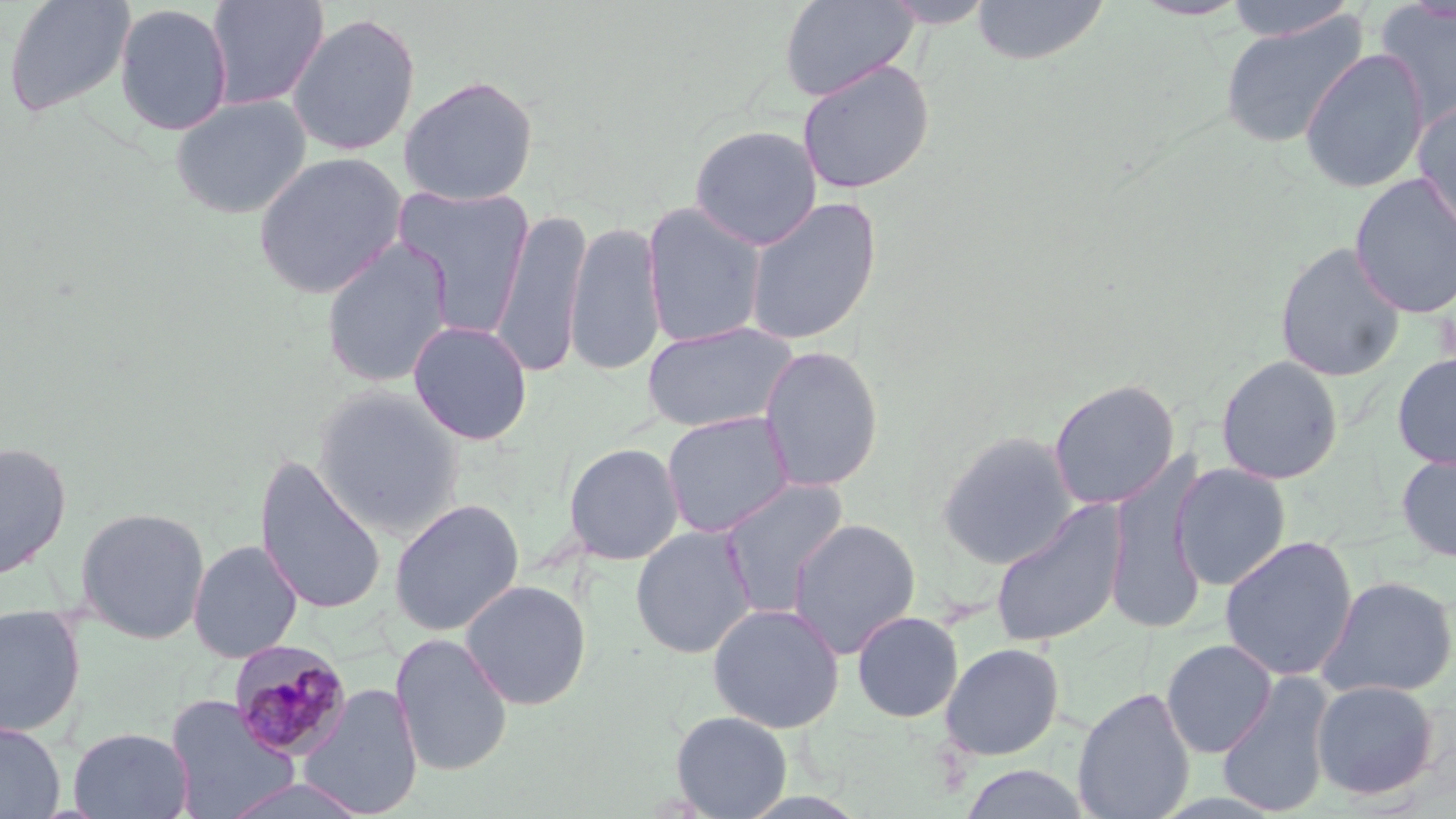
Approximate bounding boxes as (x1, y1, x2, y2) in pixels. Plasmodium malariae-infected red blood cell locations: (226, 639, 351, 761). Uninfected red blood cell locations: (3, 0, 136, 119), (778, 0, 918, 101), (971, 0, 1110, 66), (1221, 0, 1359, 41), (206, 1, 330, 110), (880, 1, 996, 29), (114, 3, 233, 136), (1375, 3, 1456, 129), (286, 11, 421, 156), (1219, 13, 1369, 149), (1299, 47, 1430, 193), (797, 59, 935, 195), (399, 75, 539, 206), (169, 94, 312, 219), (1413, 99, 1456, 239), (689, 124, 822, 250), (252, 151, 408, 299), (1349, 173, 1456, 318), (392, 184, 536, 336), (743, 195, 882, 346), (641, 202, 767, 349), (490, 207, 592, 379), (565, 221, 666, 378), (320, 238, 454, 388), (1274, 241, 1406, 383), (407, 320, 533, 446), (640, 321, 799, 435), (758, 344, 884, 493), (1392, 351, 1456, 470), (1215, 355, 1343, 485), (1047, 378, 1180, 510), (311, 385, 465, 536), (661, 411, 795, 538), (936, 430, 1078, 570), (0, 441, 72, 580), (563, 442, 685, 565), (1396, 449, 1456, 563), (1105, 450, 1209, 635), (254, 454, 387, 617), (1172, 463, 1291, 590), (718, 478, 850, 617), (389, 498, 525, 636), (990, 501, 1128, 648), (74, 506, 211, 644), (787, 518, 921, 659), (630, 525, 757, 659), (1219, 535, 1358, 681), (188, 539, 303, 663), (1315, 574, 1456, 700), (460, 579, 592, 710), (707, 602, 845, 733), (0, 603, 86, 739), (852, 610, 963, 722), (390, 633, 513, 776), (1160, 639, 1278, 758), (940, 642, 1065, 760), (1216, 671, 1336, 818), (1311, 679, 1440, 799), (299, 684, 424, 818), (1072, 687, 1196, 819), (164, 695, 299, 819), (671, 710, 792, 818), (0, 721, 65, 819), (68, 727, 194, 819), (957, 764, 1096, 819), (218, 777, 370, 819). Slide-level diagnosis: Plasmodium malariae. Image is 1456×819 pixels. May-Grünwald-Giemsa-stained preparation. 1000x magnification. Thin blood smear. One field of a larger specimen. Light microscopy.